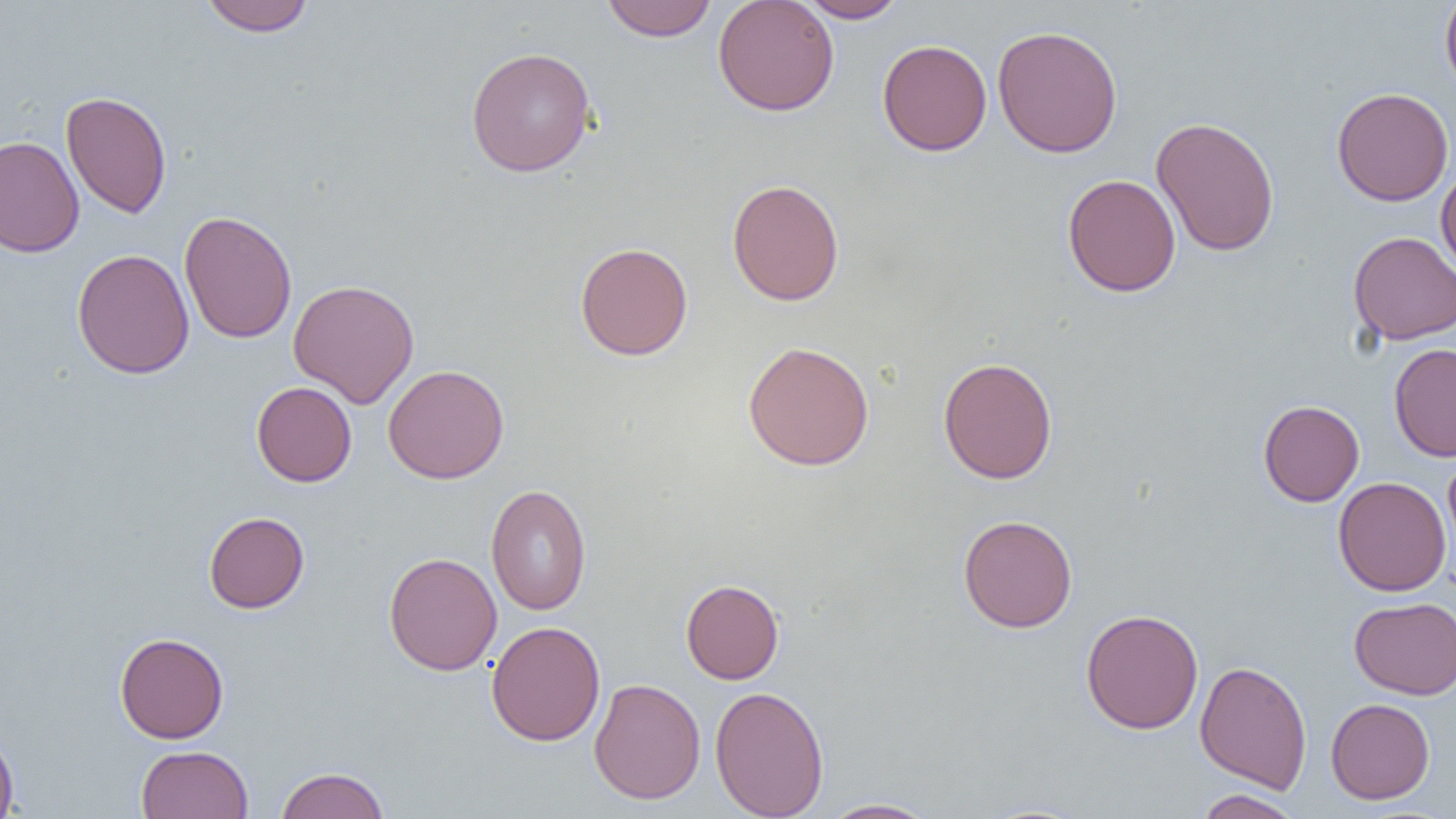
Summary:
  - Coordinate format: approximate bounding boxes as (x1,y1)-(x2,y2) corner pairs in pixels
  - Uninfected red blood cell locations: (198,0)-(316,36), (601,0)-(718,42), (712,0)-(840,116), (796,0)-(907,23), (1440,0)-(1456,97), (992,24)-(1123,158), (877,39)-(992,156), (465,46)-(597,177), (1331,87)-(1454,206), (61,90)-(172,218), (1151,116)-(1280,257), (0,135)-(84,258), (1436,163)-(1456,278), (1062,173)-(1181,297), (727,178)-(845,306), (178,210)-(297,344), (1348,231)-(1456,345), (575,241)-(693,361), (72,248)-(195,379), (288,279)-(420,408), (742,340)-(875,471), (1388,343)-(1456,461), (938,357)-(1058,484), (382,364)-(509,484), (251,381)-(357,487), (1258,400)-(1364,506), (1443,451)-(1456,573), (1333,476)-(1451,596), (485,484)-(592,615), (204,511)-(309,613), (958,514)-(1077,633), (384,551)-(502,676), (681,579)-(784,684), (1349,596)-(1456,700), (1080,608)-(1204,734), (486,621)-(606,746), (114,632)-(229,743), (1194,660)-(1312,792), (588,678)-(706,804), (710,685)-(829,819), (1326,698)-(1435,804), (0,726)-(19,819), (136,745)-(253,818), (275,766)-(390,819), (1193,789)-(1304,819), (818,798)-(940,818)
  - Slide-level diagnosis: no evidence of blood parasites
  - Preparation: thin blood smear
  - Magnification: 1000x
  - Image size: 1456×819 pixels
  - Modality: light microscopy
  - Field of view: single